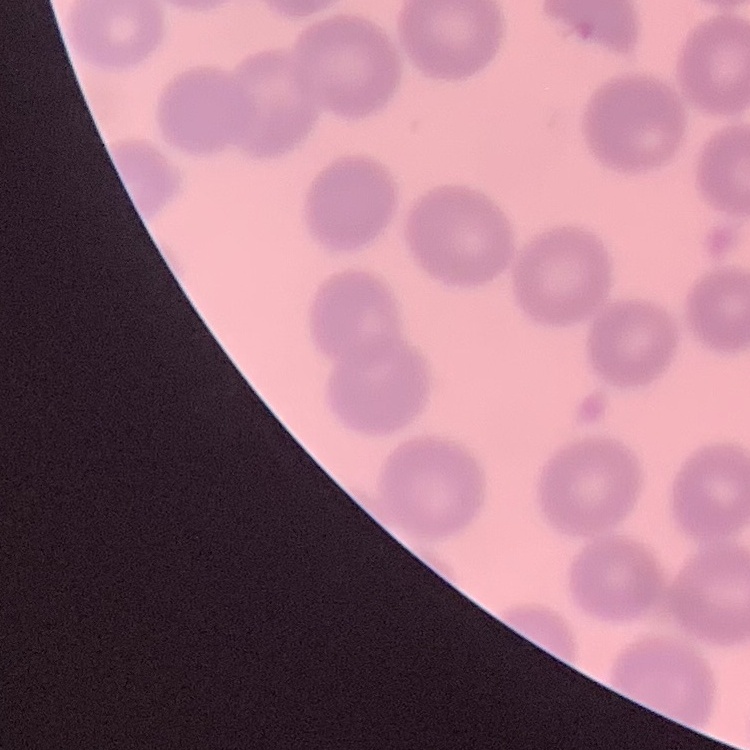

The erythrocytes exhibit no rouleaux formation. Field's or Giemsa stain. One tile cut from a larger photomicrograph. Thin blood smear.